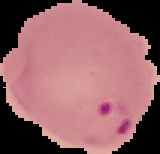 From a thin blood smear. Image is 160×154 pixels. Cell region segmented out of the field of view; the surrounding area is masked to black. Result: malaria parasites identified.